Assess this cell for malaria.
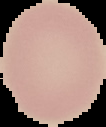
Uninfected.

Summary:
  - Image type: segmented cell region on a black background
  - Image size: 106×127 pixels
  - Preparation: thin blood film